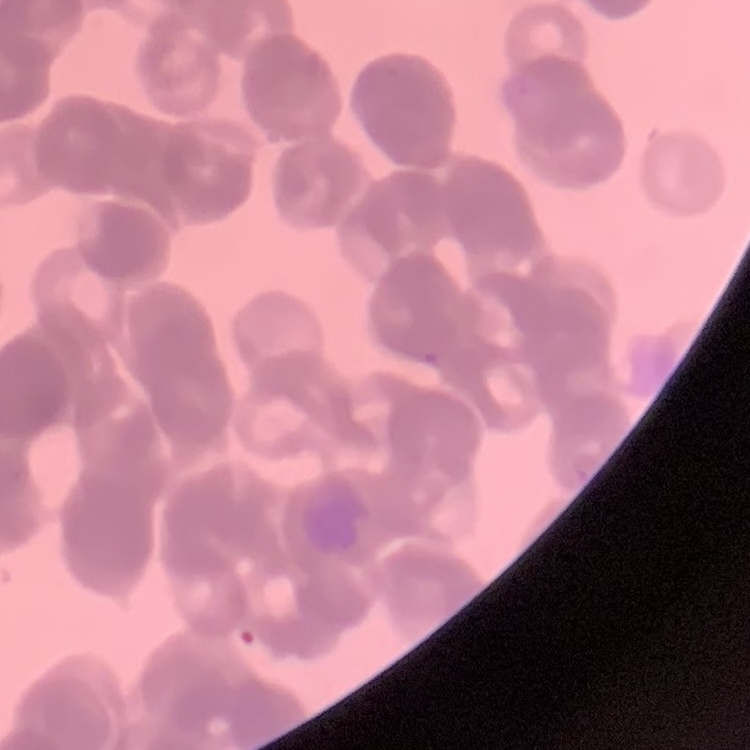
The red blood cells exhibit rouleaux formation. Square crop of a larger photomicrograph. Thin blood smear. Field's or Giemsa stain.